Give the position of every malaria parasite.
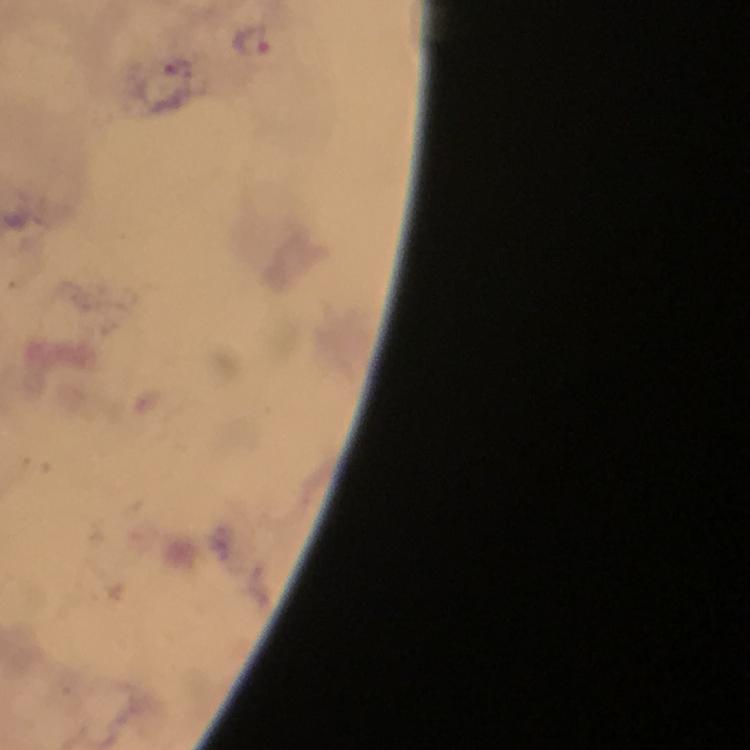

Approximate centers as {x, y} in pixels.
Malaria parasites: {251, 38}.

Summary:
  - Preparation: thick blood film
  - Image size: 750×750 pixels
  - Stain: Giemsa
  - Magnification: 100x
  - Immersion oil: applied
  - Context: from a diagnostic examination for malaria
  - Capture: smartphone photograph through a microscope
  - Cropped from: a single field of view